Assess the morphology of the erythrocytes.
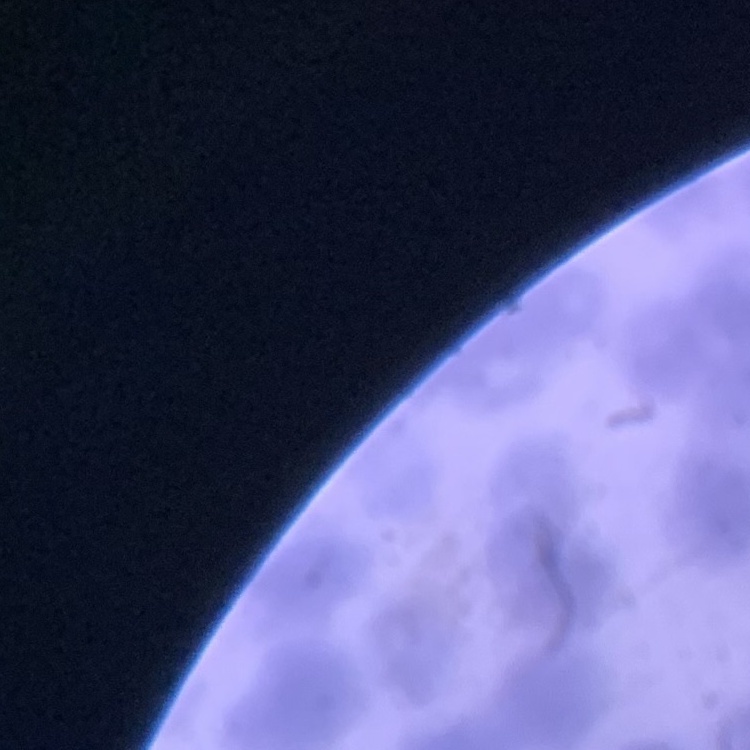

Rouleaux formation.

{
  "stain": "Field's or Giemsa",
  "preparation": "thin blood smear",
  "image_type": "one tile cut from a larger photomicrograph"
}